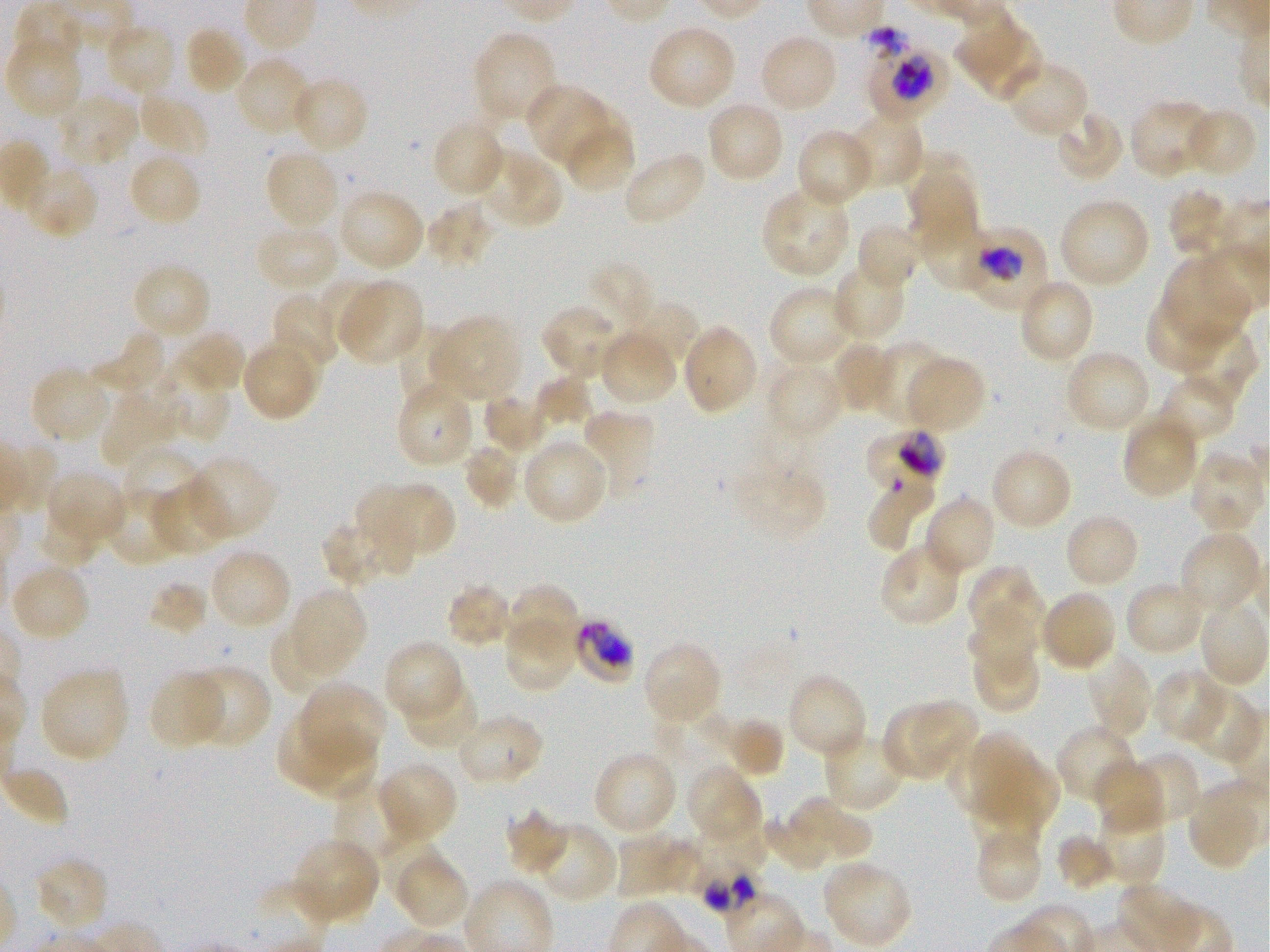
Approximate bounding boxes as [x1, y1, x2, y2] in pixels. Not every red blood cell is marked. A life-cycle stage — or a range of stages, where the recorded stages span more than one — follows each staged infected red blood cell. Locations of infected red blood cells: [861, 24, 946, 119] trophozoite; [972, 225, 1047, 311] early trophozoite; [863, 430, 947, 486] late trophozoite; [576, 619, 633, 680]; [693, 862, 763, 918]. Locations of uninfected red blood cells: [18, 3, 87, 65], [954, 13, 1042, 101], [103, 22, 177, 99], [647, 23, 737, 111], [183, 24, 249, 95], [472, 30, 559, 127], [757, 32, 839, 114], [4, 35, 85, 120], [235, 56, 315, 138], [1003, 60, 1088, 140], [290, 76, 369, 156], [524, 84, 609, 166], [134, 91, 209, 162], [56, 92, 141, 169], [1128, 99, 1218, 180], [705, 100, 785, 184], [559, 105, 631, 170], [1182, 107, 1257, 179], [1054, 108, 1126, 184], [845, 110, 924, 190], [432, 119, 507, 199], [795, 129, 877, 209], [569, 131, 631, 192], [477, 148, 564, 231], [264, 149, 342, 233], [902, 149, 977, 212], [622, 150, 708, 226], [126, 151, 202, 230], [22, 165, 99, 240], [906, 172, 975, 256], [761, 185, 852, 279], [337, 188, 425, 273], [1167, 188, 1238, 257], [1057, 198, 1151, 290], [424, 202, 495, 269], [855, 220, 924, 292], [254, 224, 341, 294], [928, 225, 991, 290], [1161, 254, 1253, 348], [831, 261, 907, 342], [130, 262, 212, 342], [589, 263, 655, 333], [322, 277, 382, 349], [335, 278, 425, 367], [1017, 278, 1095, 366], [768, 284, 856, 370], [269, 290, 342, 372], [1147, 298, 1230, 375], [622, 301, 698, 370], [540, 303, 625, 381], [428, 315, 522, 403], [393, 320, 463, 402], [681, 324, 759, 415], [1172, 324, 1259, 407], [169, 329, 247, 396], [598, 329, 678, 407], [89, 330, 170, 397], [262, 333, 326, 398], [830, 340, 898, 414], [872, 340, 946, 424], [244, 347, 312, 421], [1063, 348, 1151, 434], [903, 355, 986, 434], [765, 361, 844, 440], [29, 365, 113, 445], [153, 371, 231, 444], [1155, 373, 1239, 448], [535, 375, 593, 428], [394, 381, 477, 470], [99, 385, 186, 467], [482, 394, 548, 457], [581, 408, 655, 500], [1121, 413, 1200, 500], [521, 435, 611, 526], [463, 440, 523, 509], [120, 446, 206, 519], [990, 447, 1073, 530], [1187, 449, 1266, 535], [726, 455, 830, 545], [184, 456, 275, 543], [44, 469, 127, 550], [388, 480, 454, 556], [151, 481, 233, 559], [868, 482, 936, 550], [105, 485, 185, 567], [354, 485, 418, 573], [922, 494, 997, 578], [38, 508, 103, 570], [1063, 513, 1141, 590], [321, 523, 393, 586], [1178, 530, 1264, 617], [879, 541, 964, 626], [207, 547, 293, 632], [10, 563, 92, 642], [967, 565, 1043, 641], [148, 581, 209, 637], [1123, 581, 1205, 657], [447, 582, 517, 648], [504, 584, 579, 641], [285, 585, 366, 680], [1040, 589, 1117, 673], [1198, 599, 1269, 689], [965, 600, 1039, 683], [504, 622, 576, 691], [267, 631, 312, 692], [384, 640, 465, 723], [641, 640, 723, 722], [971, 651, 1037, 715], [1086, 653, 1154, 741], [190, 665, 271, 748], [38, 666, 130, 763], [147, 668, 228, 750], [1151, 668, 1230, 745], [784, 671, 868, 761], [403, 676, 481, 752], [301, 681, 386, 762], [1185, 685, 1263, 766], [912, 698, 982, 765], [656, 702, 736, 770], [881, 706, 954, 782], [455, 713, 545, 787], [723, 718, 784, 777], [278, 720, 347, 787], [1056, 724, 1139, 806], [303, 726, 376, 799], [822, 729, 906, 812], [973, 729, 1034, 802], [592, 750, 678, 836], [1123, 751, 1201, 830], [944, 756, 1007, 811], [1093, 759, 1168, 836], [375, 760, 459, 846], [689, 761, 761, 839], [1001, 762, 1061, 824], [0, 767, 68, 827], [338, 778, 426, 861], [1191, 781, 1259, 867], [795, 794, 839, 848], [972, 796, 1011, 857], [1004, 796, 1041, 853], [1094, 800, 1166, 888], [506, 809, 569, 874], [816, 813, 872, 860], [760, 814, 830, 869], [698, 818, 770, 872], [530, 821, 617, 904], [379, 830, 444, 901], [615, 831, 670, 901], [1055, 833, 1114, 892], [290, 835, 380, 925], [976, 835, 1043, 904], [660, 840, 708, 892], [395, 851, 467, 927], [34, 856, 111, 934], [820, 858, 912, 949]. 100x objective under oil immersion, numerical aperture 1.25. Thin blood smear. Giemsa stain. One field from this slide. Image is 1270×952 pixels. Static in-vitro culture of P. falciparum strain 3D7. Donor blood group O+.